Describe the morphology of the red blood cells.
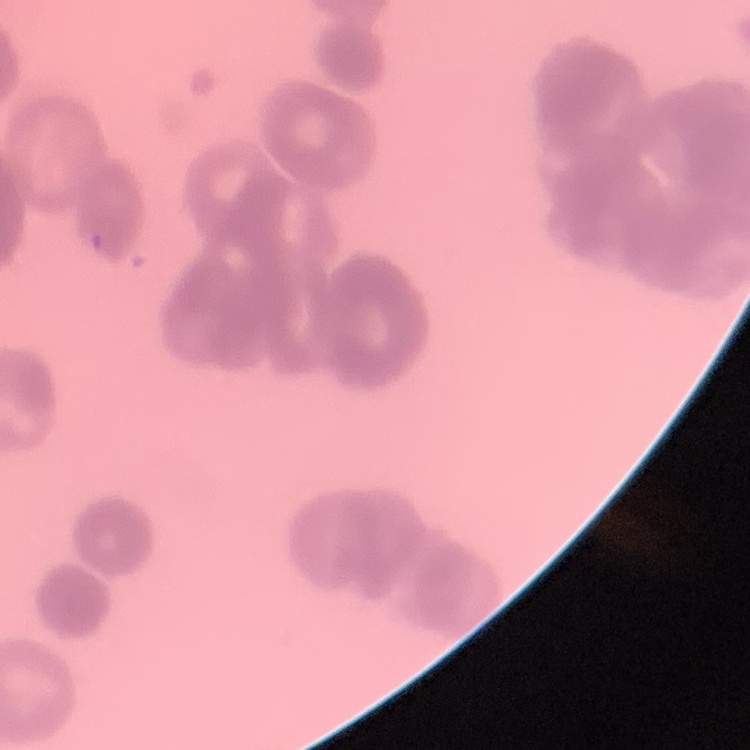
Rouleaux formation.

Summary:
  - Stain: Field's or Giemsa
  - Preparation: thin peripheral smear
  - Image type: square crop of a larger photomicrograph